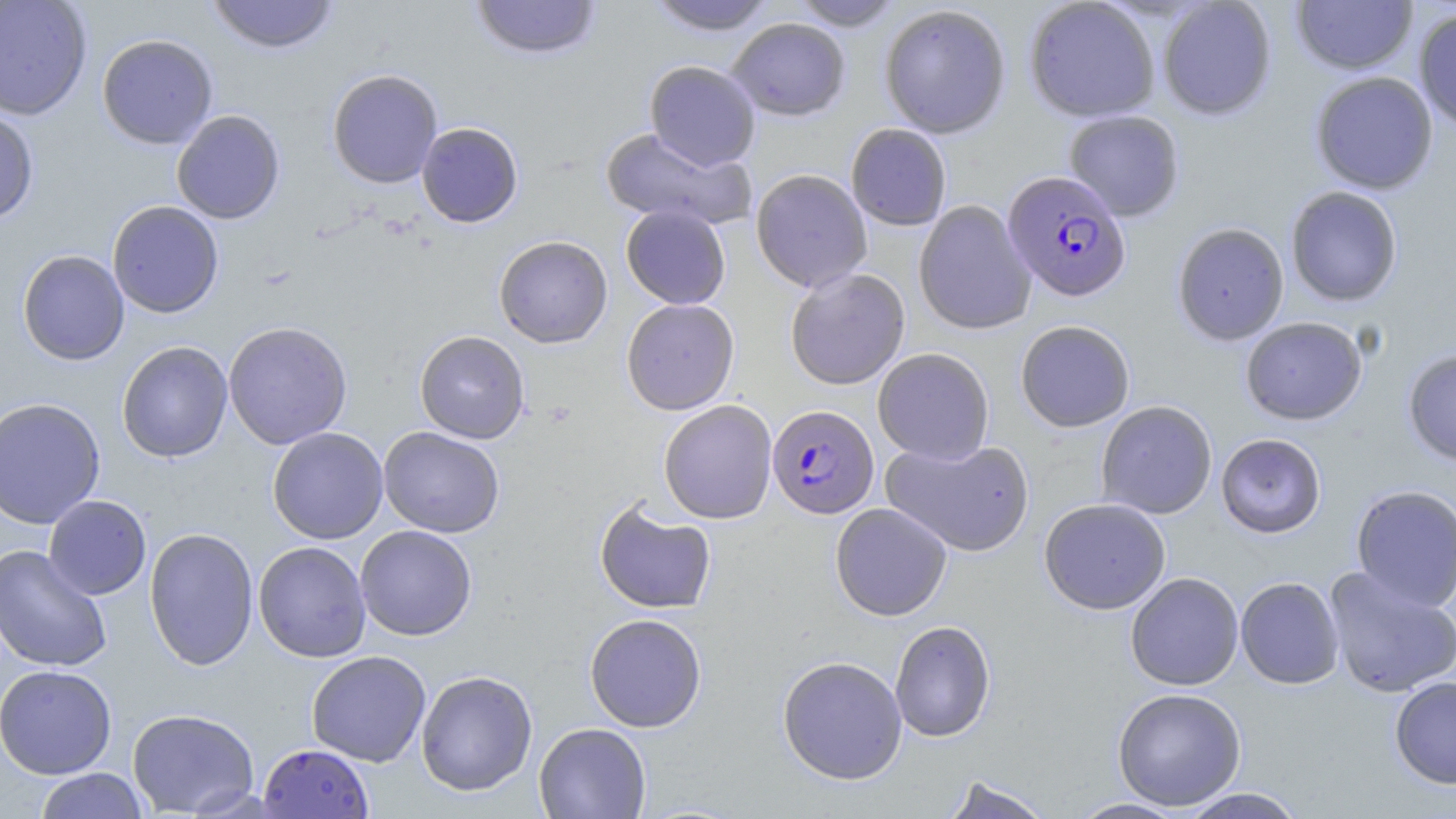
slide_level_diagnosis: Plasmodium falciparum
modality: optical microscopy
preparation: thin blood film
plasmodium_falciparum_infected_red_blood_cell_locations: 'approximate bounding boxes as named x1/y1/x2/y2 corners in pixels: (x1=1003, y1=171, x2=1131, y2=302), (x1=767, y1=404, x2=878, y2=518)'
stain: May-Grünwald-Giemsa
magnification: 1000x
uninfected_red_blood_cell_locations: 'approximate bounding boxes as named x1/y1/x2/y2 corners in pixels: (x1=0, y1=0, x2=92, y2=120), (x1=207, y1=0, x2=340, y2=54), (x1=470, y1=0, x2=603, y2=61), (x1=645, y1=0, x2=776, y2=35), (x1=787, y1=0, x2=905, y2=31), (x1=1024, y1=0, x2=1160, y2=122), (x1=1157, y1=1, x2=1276, y2=120), (x1=1291, y1=1, x2=1417, y2=74), (x1=879, y1=4, x2=1011, y2=138), (x1=1413, y1=7, x2=1456, y2=131), (x1=727, y1=18, x2=850, y2=121), (x1=97, y1=33, x2=218, y2=150), (x1=644, y1=60, x2=761, y2=171), (x1=327, y1=68, x2=443, y2=188), (x1=1310, y1=71, x2=1438, y2=195), (x1=0, y1=108, x2=39, y2=224), (x1=171, y1=110, x2=285, y2=224), (x1=1063, y1=110, x2=1184, y2=221), (x1=417, y1=122, x2=523, y2=228), (x1=846, y1=123, x2=951, y2=231), (x1=599, y1=127, x2=754, y2=231), (x1=751, y1=169, x2=872, y2=292), (x1=1285, y1=186, x2=1403, y2=306), (x1=107, y1=200, x2=224, y2=319), (x1=913, y1=200, x2=1036, y2=335), (x1=621, y1=205, x2=731, y2=309), (x1=1172, y1=222, x2=1289, y2=346), (x1=494, y1=235, x2=612, y2=348), (x1=17, y1=249, x2=129, y2=366), (x1=785, y1=268, x2=910, y2=390), (x1=621, y1=298, x2=740, y2=415), (x1=1240, y1=317, x2=1368, y2=425), (x1=1015, y1=320, x2=1135, y2=432), (x1=223, y1=321, x2=353, y2=450), (x1=414, y1=330, x2=530, y2=444), (x1=117, y1=341, x2=233, y2=463), (x1=872, y1=347, x2=994, y2=464), (x1=1402, y1=349, x2=1456, y2=466), (x1=0, y1=397, x2=106, y2=529), (x1=658, y1=399, x2=777, y2=524), (x1=1096, y1=401, x2=1217, y2=519), (x1=378, y1=426, x2=505, y2=538), (x1=267, y1=427, x2=388, y2=544), (x1=1216, y1=433, x2=1326, y2=538), (x1=881, y1=437, x2=1035, y2=557), (x1=1351, y1=484, x2=1456, y2=612), (x1=43, y1=495, x2=152, y2=599), (x1=1039, y1=498, x2=1171, y2=614), (x1=594, y1=500, x2=717, y2=614), (x1=830, y1=503, x2=952, y2=621), (x1=355, y1=525, x2=477, y2=641), (x1=144, y1=527, x2=259, y2=671), (x1=253, y1=541, x2=372, y2=663), (x1=0, y1=544, x2=112, y2=672), (x1=1323, y1=566, x2=1456, y2=698), (x1=1125, y1=572, x2=1244, y2=690), (x1=1236, y1=576, x2=1344, y2=689), (x1=584, y1=613, x2=707, y2=732), (x1=890, y1=620, x2=996, y2=742), (x1=306, y1=650, x2=431, y2=767), (x1=777, y1=655, x2=907, y2=785), (x1=0, y1=664, x2=116, y2=779), (x1=415, y1=669, x2=538, y2=797), (x1=1389, y1=676, x2=1456, y2=789), (x1=1112, y1=687, x2=1247, y2=810), (x1=127, y1=708, x2=260, y2=817), (x1=534, y1=722, x2=651, y2=818), (x1=259, y1=744, x2=373, y2=818), (x1=35, y1=768, x2=148, y2=819), (x1=939, y1=775, x2=1057, y2=819), (x1=1178, y1=787, x2=1309, y2=818), (x1=1069, y1=797, x2=1189, y2=818)'
image_size: 1456×819 pixels
field_of_view: single